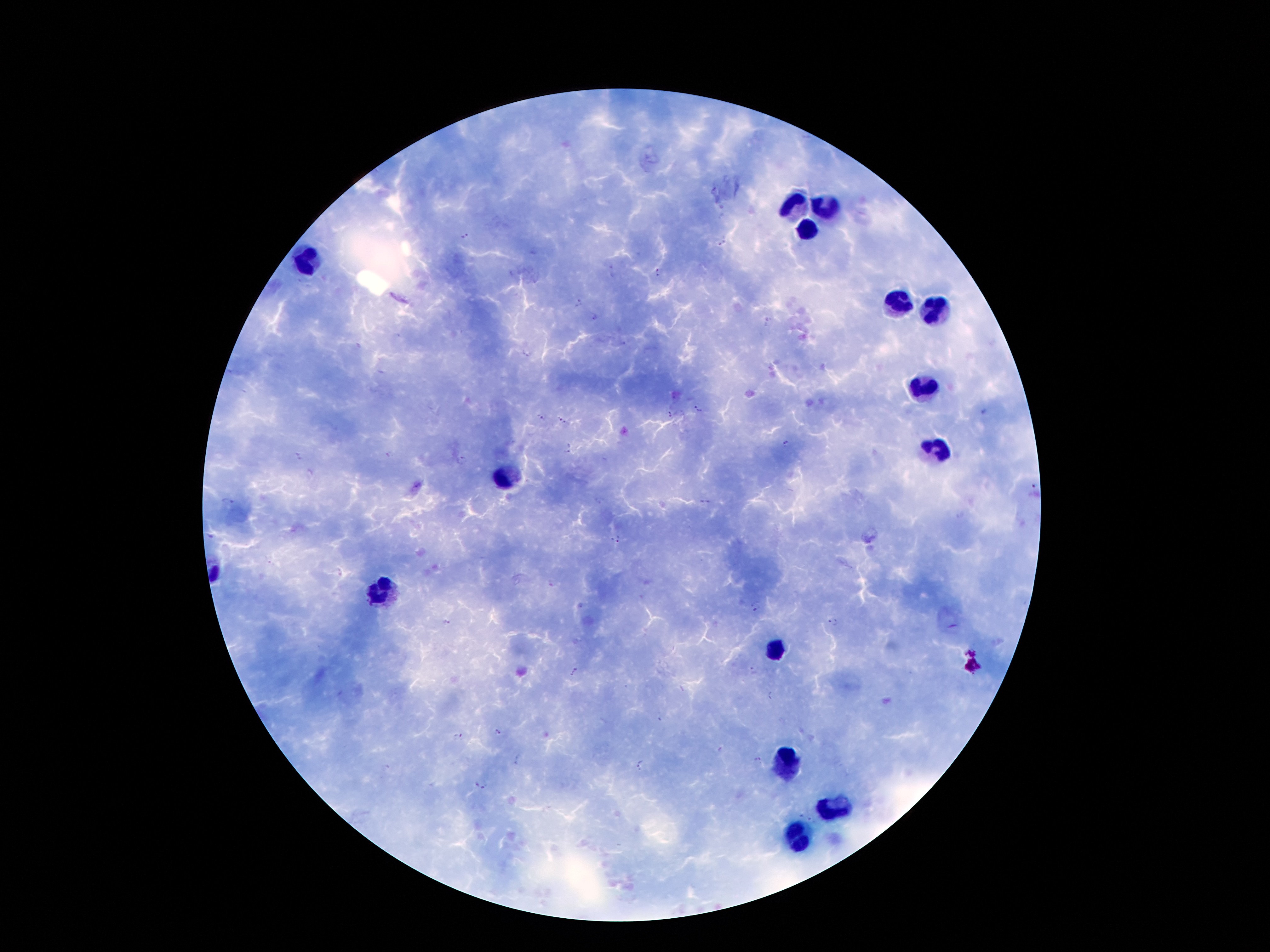
coordinate format = approximate centers as {x, y} in pixels
leukocyte locations = {794, 204}, {825, 207}, {806, 227}, {310, 260}, {895, 302}, {937, 311}, {920, 386}, {937, 451}, {503, 481}, {380, 588}, {772, 644}, {786, 767}, {834, 806}, {797, 840}
Plasmodium parasite locations = {466, 236}, {723, 243}, {614, 270}, {657, 274}, {578, 302}, {593, 317}, {766, 322}, {526, 353}, {699, 409}, {669, 413}, {541, 418}, {562, 420}, {787, 443}, {570, 448}, {296, 456}, {387, 456}, {461, 459}, {1035, 485}, {228, 501}, {704, 502}, {615, 539}, {755, 604}, {445, 622}, {833, 623}, {752, 669}, {575, 672}, {772, 694}, {659, 717}, {497, 733}, {457, 736}, {518, 760}, {755, 761}, {640, 765}, {481, 785}
patient malaria status = infected with Plasmodium falciparum
capture = smartphone through the microscope eyepiece
field of view = one from this slide
image size = 1270×952 pixels
stain = Giemsa
magnification = 100x
preparation = thick blood film